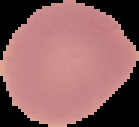

Summary:
  - Malaria status: uninfected
  - Image type: cell region segmented out of the field of view; surrounding area masked to black
  - Image size: 139×127 pixels
  - Preparation: thin blood smear